Identify the cell.
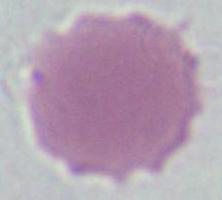

An erythrocyte.

1000x magnification. Micrograph.